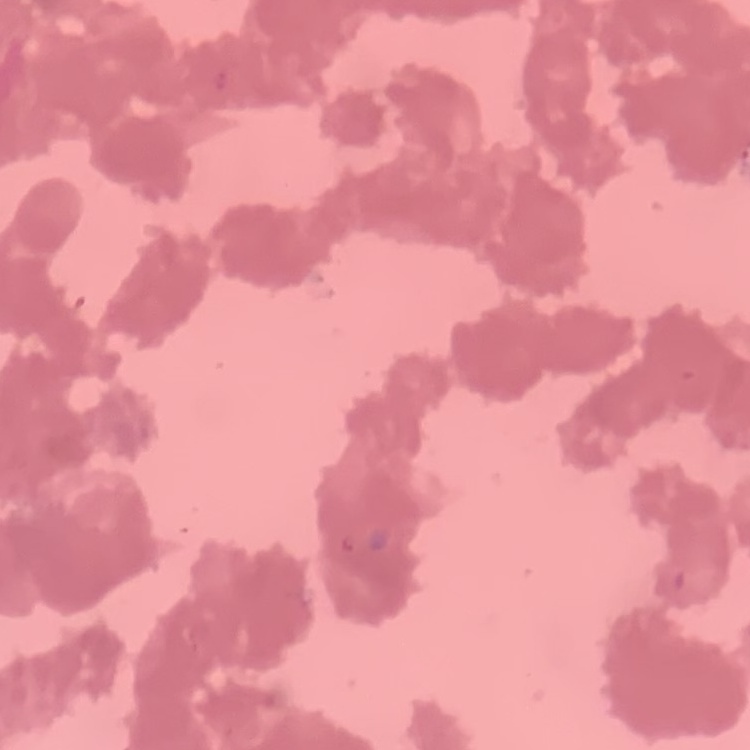 The erythrocytes show rouleaux formation. Stained with either Field's or Giemsa. Thin blood film. One tile cut from a larger photomicrograph.